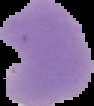

image type = segmented cell region with the area outside set to black
preparation = thin blood smear
result = malaria parasites detected
image size = 94×106 pixels